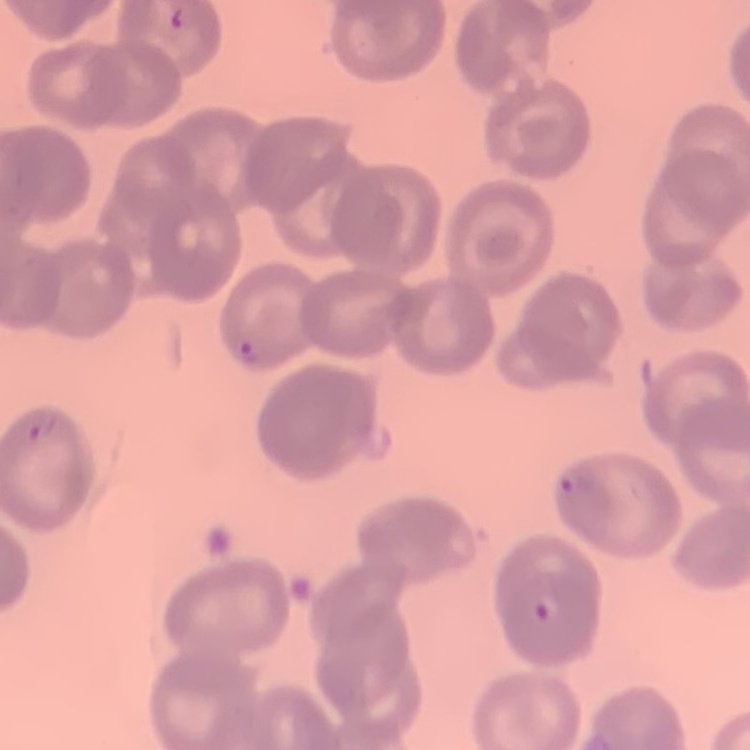 The erythrocytes show no rouleaux formation. Square crop of a larger photomicrograph. Thin blood smear. Stained with either Field's or Giemsa.